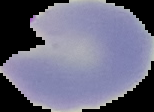

Summary:
  - Image type: segmented cell region with the area outside set to black
  - Malaria status: parasitized
  - Image size: 154×112 pixels
  - Preparation: thin blood film